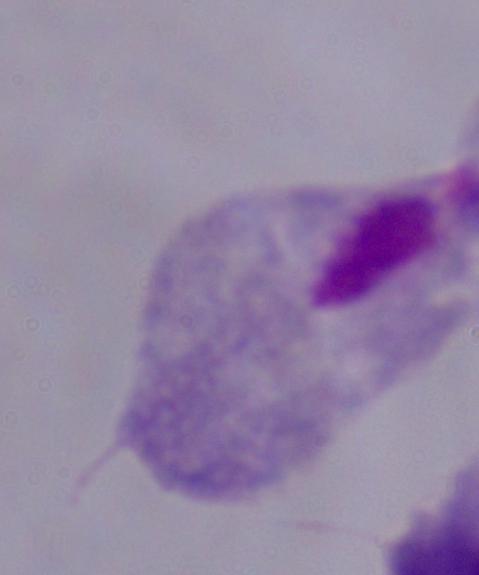 1000x magnification. Photomicrograph. A trichomonad is seen.